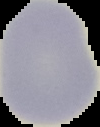 Result: no Plasmodium parasites detected. Image is 100×127 pixels. From a thin blood smear. Segmented cell region on a black background.